State which cell type is depicted.
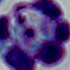

A leukocyte.

1000x magnification. Micrograph.